Classify this cell by malaria status.
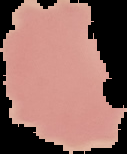
It is uninfected.

Summary:
  - Image size: 127×154 pixels
  - Image type: cell region segmented out of the field of view; surrounding area masked to black
  - Preparation: thin blood film